Classify this cell by malaria status.
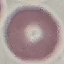
Uninfected.

Thin blood film. Giemsa-stained preparation. Automatically extracted cell patch, resized to 64 × 64 pixels. Photographed with a smartphone camera at the microscope eyepiece.